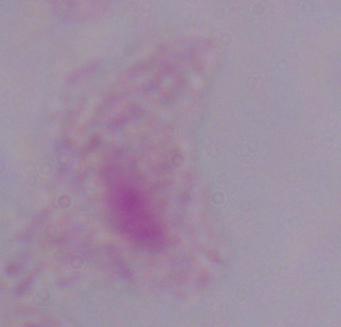

Summary:
  - Modality: micrograph
  - Identification: trichomonad
  - Magnification: 1000x